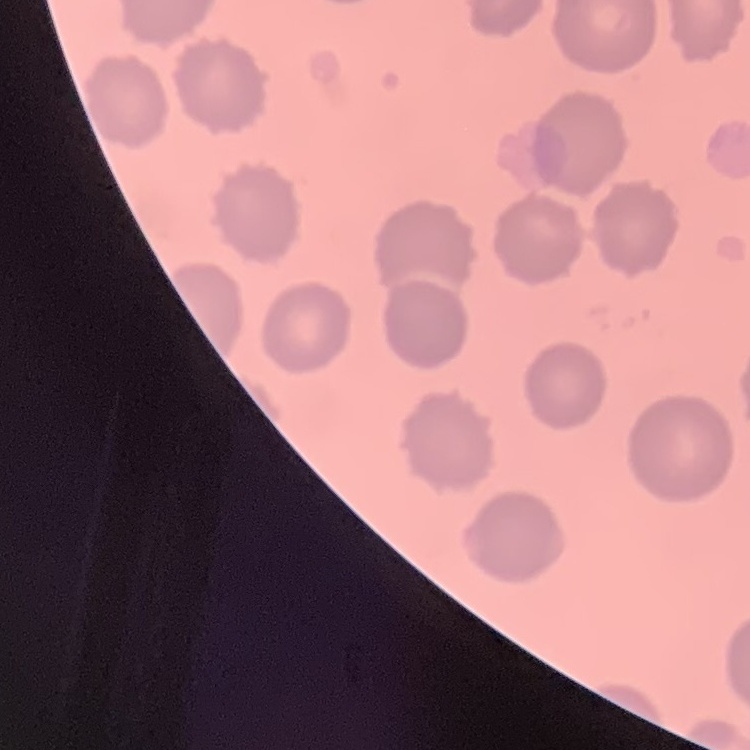
Summary:
  - Red blood cell morphology: no rouleaux formation
  - Stain: Field's or Giemsa
  - Preparation: thin blood smear
  - Image type: square crop of a larger photomicrograph